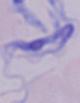

magnification = 1000x
identification = trypanosome
modality = photomicrograph